Assess this cell for malaria.
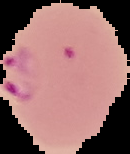

It is parasitized.

Summary:
  - Preparation: thin blood smear
  - Image size: 130×154 pixels
  - Image type: cell region segmented out of the field of view; surrounding area masked to black